Assess this cell for malaria.
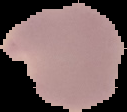

Parasitized.

From a thin blood smear. Image is 127×112 pixels. The area outside the segmented cell region is set to black.